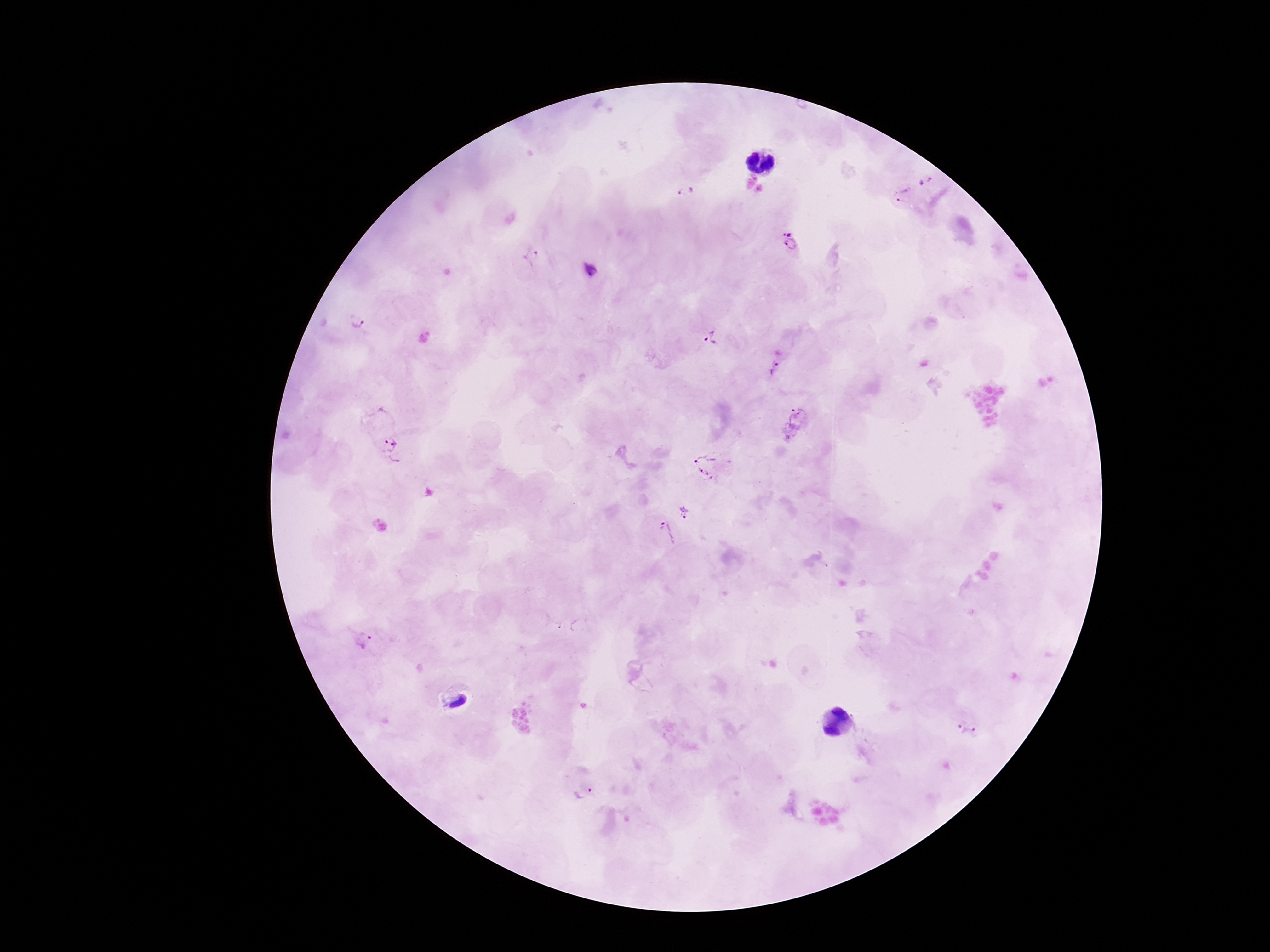

Approximate object centers, in pixels from the top-left corner.
Summary:
  - Plasmodium parasite locations: (x=925, y=182), (x=686, y=190), (x=902, y=195), (x=787, y=230), (x=792, y=246), (x=531, y=255), (x=591, y=271), (x=358, y=321), (x=712, y=336), (x=774, y=368), (x=798, y=416), (x=393, y=449), (x=710, y=464), (x=684, y=511), (x=665, y=534), (x=360, y=638), (x=968, y=728), (x=582, y=792)
  - Magnification: 100x
  - Capture: smartphone camera through the microscope eyepiece
  - Image size: 1270×952 pixels
  - Patient malaria status: infected
  - Field of view: one from this slide
  - Preparation: thick blood film
  - Stain: Giemsa